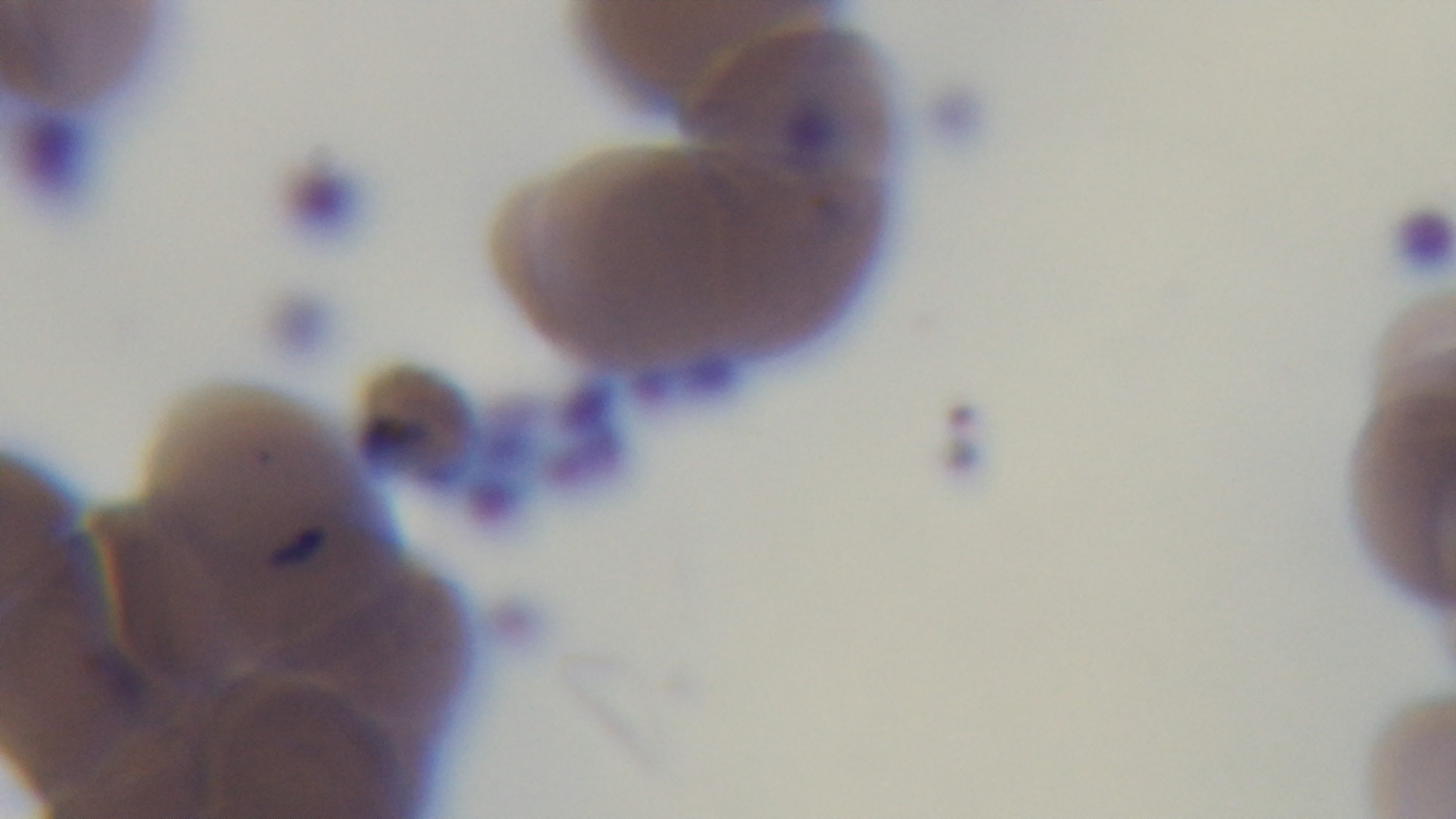
Giemsa-stained. Photomicrograph. Malaria status: infected. Mounted 4K digital camera. One field from the slide. Preparation: thin. 100x oil-immersion objective.